Outline each Plasmodium falciparum-infected red blood cell.
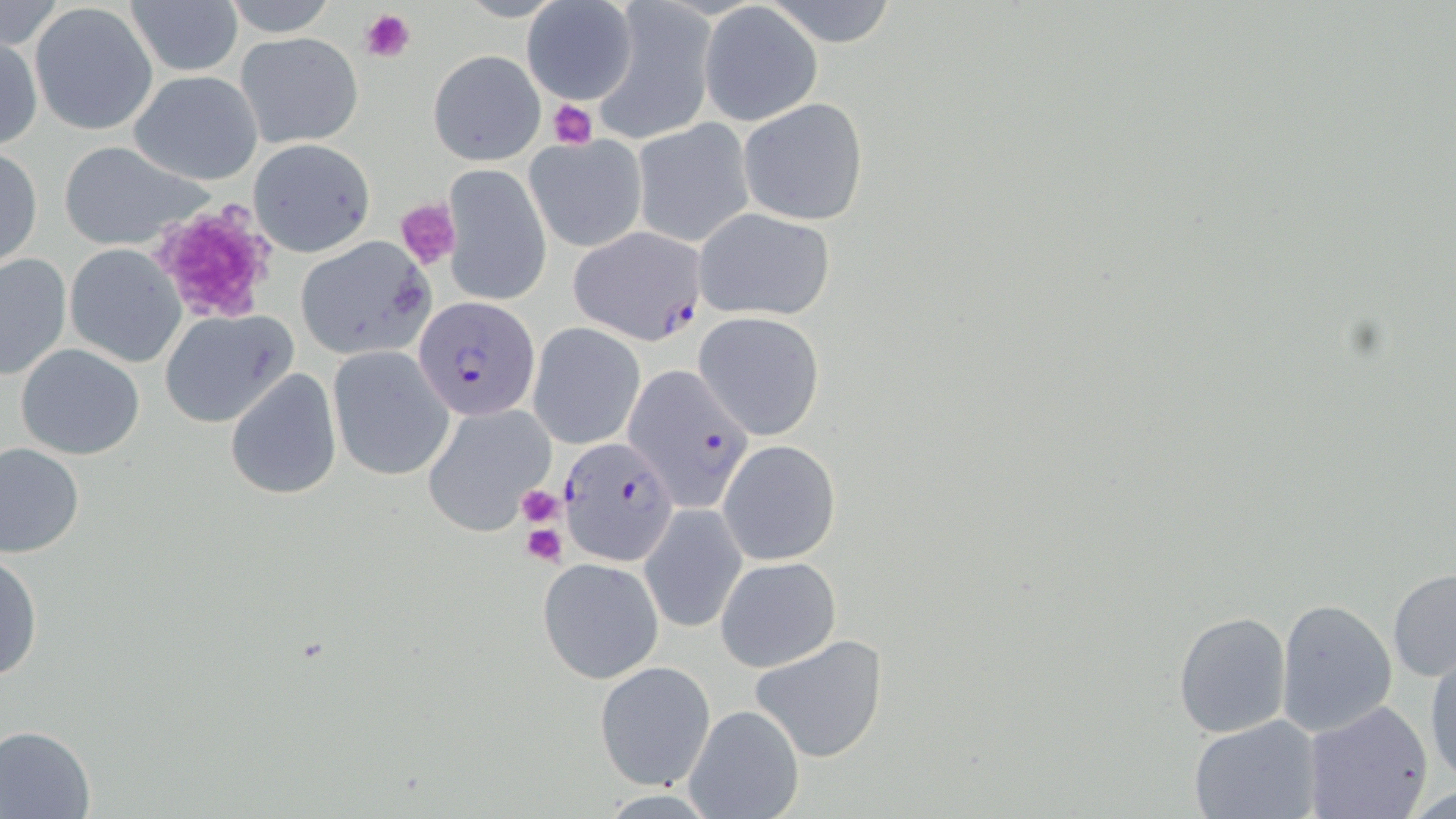

Approximate bounding boxes as (x1, y1, x2, y2) in pixels.
Plasmodium falciparum-infected red blood cells: (569, 227, 707, 344), (414, 297, 540, 423), (622, 362, 756, 514), (557, 436, 681, 568).

Summary:
  - Platelet locations: (361, 8, 417, 64), (547, 99, 596, 148), (394, 198, 462, 271), (148, 202, 279, 324), (515, 484, 565, 528), (521, 523, 567, 566)
  - Uninfected red blood cell locations: (125, 0, 243, 77), (764, 0, 901, 48), (32, 2, 159, 135), (221, 2, 344, 35), (522, 2, 641, 105), (593, 3, 715, 143), (699, 4, 822, 127), (233, 31, 364, 150), (1, 33, 42, 150), (429, 50, 544, 165), (128, 70, 264, 186), (740, 98, 868, 227), (634, 119, 755, 246), (525, 132, 648, 252), (248, 138, 376, 257), (57, 139, 213, 252), (1, 146, 43, 269), (442, 164, 552, 307), (690, 208, 835, 324), (293, 235, 434, 358), (65, 244, 186, 368), (0, 252, 71, 381), (158, 309, 299, 429), (693, 311, 826, 441), (528, 322, 645, 450), (14, 343, 146, 460), (327, 346, 455, 482), (224, 367, 342, 500), (421, 402, 554, 534), (720, 438, 841, 564), (0, 442, 85, 558), (639, 503, 748, 634), (1, 550, 41, 684), (538, 557, 664, 683), (716, 557, 841, 673), (1387, 568, 1456, 681), (1277, 598, 1398, 737), (1172, 610, 1292, 740), (751, 634, 889, 763), (1425, 653, 1456, 784), (594, 659, 717, 792), (1304, 699, 1435, 819), (682, 702, 805, 819), (1188, 714, 1321, 819), (0, 724, 97, 818)
  - Slide-level diagnosis: Plasmodium falciparum
  - Image size: 1456×819 pixels
  - Preparation: thin blood smear
  - Stain: May-Grünwald-Giemsa
  - Field of view: single
  - Magnification: 1000x
  - Modality: optical microscopy